Classify this cell by malaria status.
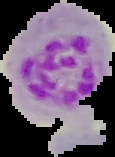
Parasitized.

Summary:
  - Image type: segmented cell region on a black background
  - Image size: 115×157 pixels
  - Preparation: thin blood film